Identify the parasite.
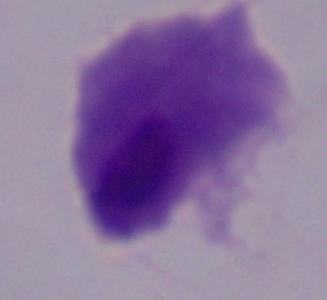

This is a trichomonad.

Captured at 1000x magnification. Photomicrograph.